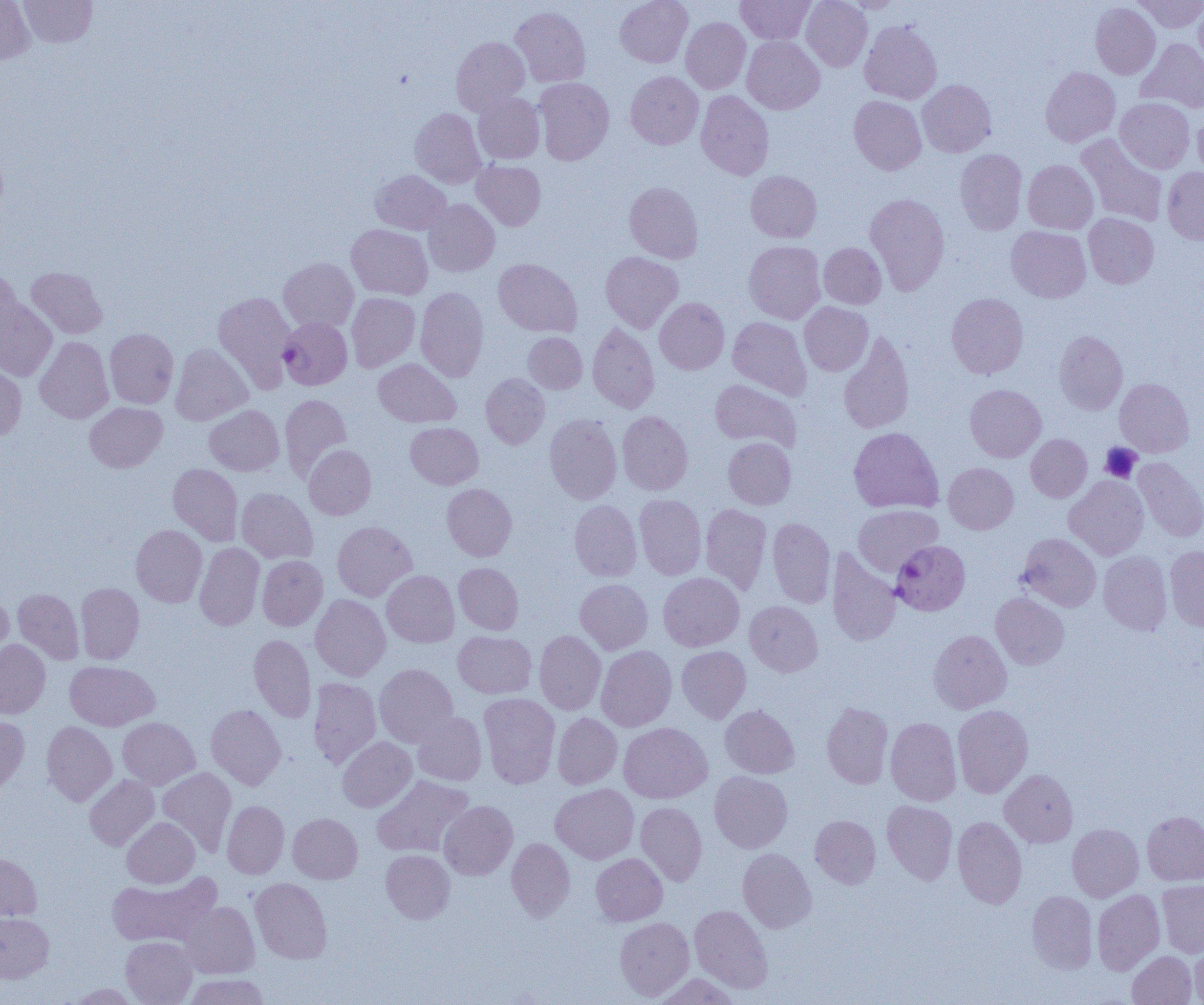 Approximate bounding boxes as [x1, y1, x2, y2] in pixels. Plasmodium falciparum-infected red blood cell locations: [279, 316, 352, 390], [890, 540, 970, 616]. Platelet locations: [1100, 443, 1142, 483]. Uninfected red blood cell locations: [0, 0, 35, 64], [19, 0, 97, 47], [615, 0, 693, 68], [736, 0, 816, 45], [801, 0, 872, 71], [838, 0, 902, 13], [1134, 0, 1204, 33], [1091, 2, 1161, 79], [1193, 2, 1204, 75], [510, 6, 590, 87], [681, 18, 751, 94], [860, 20, 942, 104], [451, 36, 529, 116], [742, 36, 824, 114], [1137, 38, 1204, 113], [1040, 67, 1120, 147], [625, 71, 704, 149], [533, 77, 614, 165], [918, 80, 996, 157], [695, 91, 774, 180], [473, 92, 545, 164], [849, 95, 926, 175], [1115, 97, 1194, 173], [410, 108, 486, 188], [1193, 112, 1204, 179], [1075, 134, 1168, 227], [955, 148, 1027, 234], [1023, 159, 1098, 233], [472, 160, 545, 230], [1162, 167, 1204, 244], [371, 170, 451, 234], [746, 170, 822, 242], [624, 182, 703, 263], [865, 193, 950, 295], [423, 199, 500, 277], [1084, 213, 1159, 288], [347, 224, 433, 299], [1006, 226, 1090, 303], [744, 240, 825, 324], [819, 242, 886, 309], [600, 251, 683, 333], [278, 257, 359, 333], [493, 258, 582, 337], [0, 266, 22, 348], [26, 266, 107, 338], [415, 286, 489, 382], [213, 291, 296, 393], [346, 292, 420, 372], [946, 293, 1028, 379], [655, 297, 729, 374], [0, 298, 57, 381], [799, 302, 873, 376], [727, 317, 811, 400], [587, 322, 659, 413], [105, 328, 179, 408], [839, 330, 915, 434], [1054, 330, 1128, 414], [523, 332, 588, 393], [35, 337, 114, 423], [170, 343, 252, 426], [373, 359, 460, 427], [0, 364, 26, 440], [481, 373, 550, 449], [1114, 378, 1194, 457], [710, 379, 800, 451], [965, 384, 1046, 462], [280, 394, 351, 480], [85, 402, 167, 472], [205, 405, 284, 475], [617, 410, 693, 495], [545, 414, 622, 504], [406, 422, 483, 489], [848, 427, 943, 513], [1026, 434, 1092, 502], [723, 437, 796, 509], [304, 445, 376, 519], [1133, 456, 1204, 542], [943, 462, 1018, 534], [168, 463, 243, 545], [1065, 476, 1148, 560], [442, 483, 517, 560], [236, 488, 318, 564], [634, 494, 706, 579], [569, 500, 641, 581], [700, 503, 772, 595], [853, 505, 943, 576], [767, 517, 836, 608], [332, 521, 416, 601], [131, 524, 207, 607], [1017, 533, 1101, 612], [195, 542, 264, 631], [1165, 546, 1204, 631], [827, 550, 901, 646], [1098, 551, 1172, 635], [257, 555, 328, 631], [454, 562, 524, 634], [382, 570, 459, 647], [658, 572, 744, 651], [575, 578, 653, 654], [76, 583, 144, 664], [13, 588, 84, 664], [0, 592, 13, 668], [991, 593, 1069, 669], [310, 594, 390, 680], [745, 600, 822, 676], [535, 630, 606, 715], [929, 630, 1012, 714], [453, 631, 536, 699], [249, 634, 316, 722], [0, 639, 50, 718], [596, 645, 676, 731], [677, 646, 750, 722], [65, 660, 159, 731], [374, 663, 457, 747], [308, 677, 381, 767], [479, 692, 560, 788], [822, 702, 893, 789], [206, 704, 285, 790], [216, 705, 286, 878], [720, 705, 799, 778], [953, 705, 1033, 798], [413, 712, 487, 785], [552, 712, 622, 789], [0, 714, 29, 795], [117, 717, 200, 789], [885, 717, 962, 806], [41, 721, 117, 806], [618, 722, 712, 803], [338, 736, 416, 812], [157, 767, 236, 855], [1000, 769, 1078, 847], [710, 771, 792, 853], [84, 775, 159, 850], [373, 775, 474, 858], [551, 783, 639, 864], [221, 800, 289, 879], [882, 800, 958, 885], [439, 801, 518, 880], [635, 802, 707, 886], [1142, 811, 1204, 885], [288, 813, 362, 884], [810, 814, 881, 888], [952, 816, 1027, 909], [122, 817, 200, 888], [1067, 823, 1144, 902], [507, 838, 575, 921], [738, 848, 816, 933], [380, 849, 455, 924], [0, 852, 43, 921], [591, 853, 667, 926], [107, 872, 221, 947], [250, 877, 332, 964], [1157, 880, 1204, 957], [1092, 889, 1165, 975], [1027, 890, 1097, 973], [179, 901, 260, 978], [690, 904, 773, 993], [0, 913, 53, 983], [614, 916, 694, 1000], [121, 936, 197, 1005], [1190, 940, 1204, 1005], [1128, 951, 1198, 1005], [654, 973, 742, 1005], [182, 974, 271, 1005], [66, 983, 140, 1004]. Slide-level diagnosis: Plasmodium falciparum. Image is 1204×1005 pixels. Light microscopy. Single field of view. Thin blood smear. 1000x magnification.